Assess this cell for malaria.
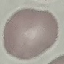
Uninfected.

image_type: automatically extracted cell patch, resized to 64 × 64 pixels
stain: Giemsa
capture: smartphone through the microscope eyepiece
preparation: thin blood smear